State the blood parasite species.
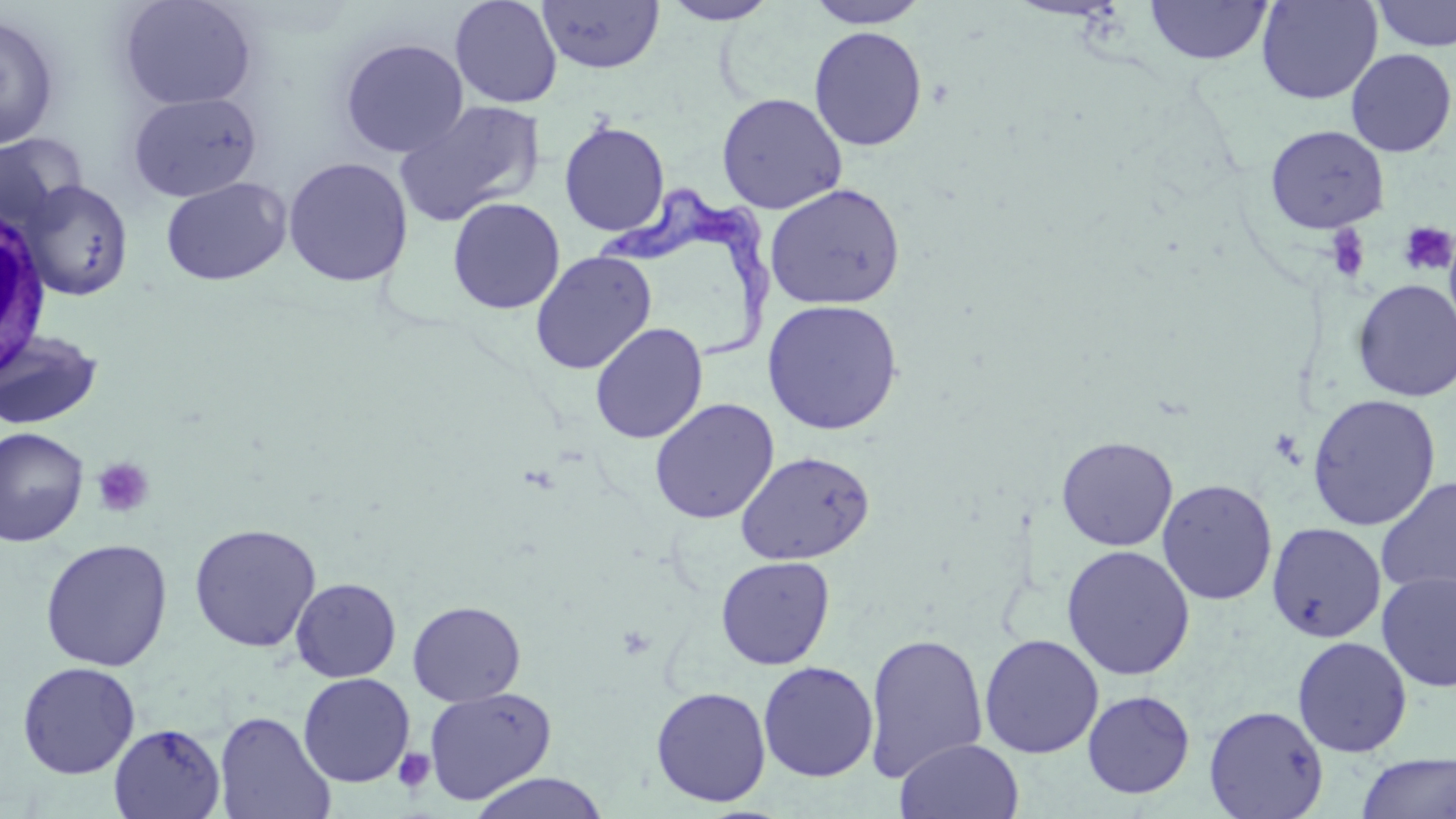
Trypanosoma brucei.

Summary:
  - Coordinate format: approximate bounding boxes as named x1/y1/x2/y2 corners in pixels
  - Platelet locations: (x1=1397, y1=221, x2=1456, y2=277), (x1=1324, y1=225, x2=1371, y2=282), (x1=1269, y1=427, x2=1304, y2=466), (x1=91, y1=456, x2=155, y2=518), (x1=393, y1=748, x2=436, y2=794)
  - White blood cell locations: (x1=0, y1=212, x2=50, y2=374)
  - Trypanosoma brucei locations: (x1=592, y1=184, x2=780, y2=361)
  - Uninfected red blood cell locations: (x1=117, y1=0, x2=258, y2=110), (x1=450, y1=0, x2=563, y2=109), (x1=660, y1=0, x2=778, y2=24), (x1=805, y1=0, x2=931, y2=29), (x1=1256, y1=0, x2=1382, y2=104), (x1=538, y1=1, x2=664, y2=74), (x1=1144, y1=1, x2=1273, y2=65), (x1=1370, y1=1, x2=1456, y2=52), (x1=0, y1=13, x2=61, y2=151), (x1=809, y1=26, x2=927, y2=151), (x1=339, y1=38, x2=468, y2=158), (x1=1345, y1=48, x2=1456, y2=157), (x1=128, y1=92, x2=262, y2=203), (x1=716, y1=92, x2=848, y2=214), (x1=393, y1=100, x2=544, y2=227), (x1=559, y1=121, x2=670, y2=236), (x1=1264, y1=125, x2=1390, y2=234), (x1=0, y1=133, x2=86, y2=235), (x1=282, y1=157, x2=413, y2=287), (x1=160, y1=176, x2=292, y2=286), (x1=22, y1=180, x2=133, y2=300), (x1=764, y1=183, x2=906, y2=309), (x1=447, y1=197, x2=565, y2=314), (x1=530, y1=250, x2=657, y2=375), (x1=1351, y1=279, x2=1456, y2=401), (x1=763, y1=298, x2=903, y2=435), (x1=590, y1=322, x2=708, y2=444), (x1=0, y1=328, x2=104, y2=430), (x1=1307, y1=394, x2=1441, y2=531), (x1=649, y1=399, x2=779, y2=524), (x1=0, y1=427, x2=88, y2=546), (x1=1056, y1=435, x2=1178, y2=551), (x1=735, y1=450, x2=875, y2=565), (x1=1376, y1=476, x2=1456, y2=596), (x1=1156, y1=478, x2=1277, y2=605), (x1=1266, y1=522, x2=1387, y2=643), (x1=188, y1=523, x2=322, y2=653), (x1=39, y1=538, x2=173, y2=672), (x1=1060, y1=545, x2=1196, y2=680), (x1=715, y1=555, x2=836, y2=670), (x1=1376, y1=571, x2=1456, y2=692), (x1=290, y1=577, x2=401, y2=682), (x1=408, y1=600, x2=526, y2=706), (x1=863, y1=632, x2=988, y2=782), (x1=978, y1=633, x2=1104, y2=758), (x1=1291, y1=635, x2=1413, y2=757), (x1=17, y1=661, x2=141, y2=779), (x1=758, y1=661, x2=878, y2=782), (x1=298, y1=673, x2=415, y2=787), (x1=651, y1=686, x2=771, y2=807), (x1=423, y1=687, x2=557, y2=805), (x1=1082, y1=690, x2=1195, y2=798), (x1=1082, y1=698, x2=1327, y2=810), (x1=1204, y1=705, x2=1329, y2=819), (x1=214, y1=711, x2=336, y2=819), (x1=109, y1=723, x2=225, y2=819), (x1=894, y1=738, x2=1025, y2=819), (x1=1356, y1=752, x2=1455, y2=819), (x1=467, y1=772, x2=611, y2=819)
  - Modality: light microscopy
  - Field of view: one of a larger specimen
  - Stain: May-Grünwald-Giemsa
  - Preparation: thin blood film
  - Image size: 1456×819 pixels
  - Magnification: 1000x